Describe the morphology of the red blood cells.
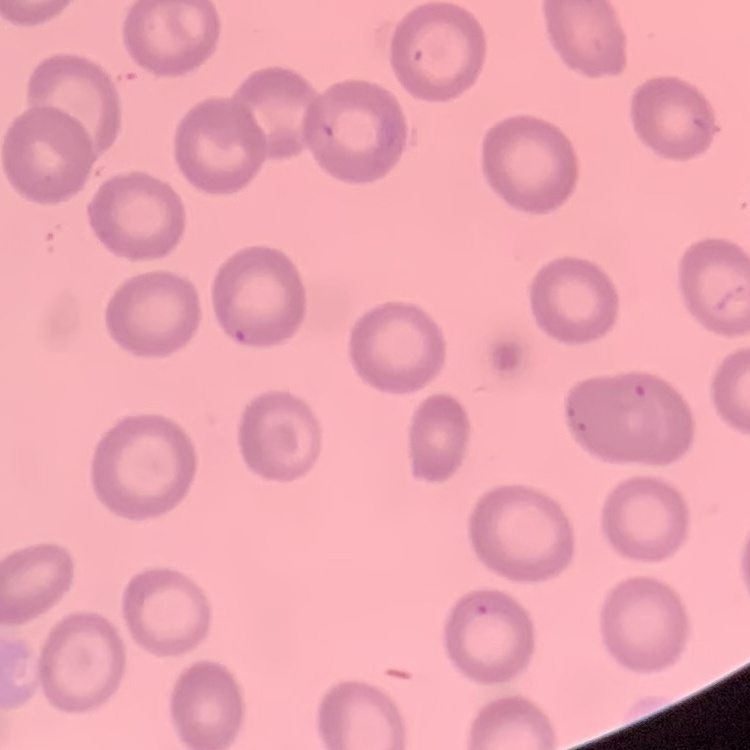

No rouleaux formation.

Summary:
  - Image type: one tile cut from a larger photomicrograph
  - Preparation: thin peripheral smear
  - Stain: Field's or Giemsa